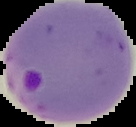

image size = 136×127 pixels
preparation = thin blood film
image type = segmented cell region with the area outside set to black
malaria status = parasitized